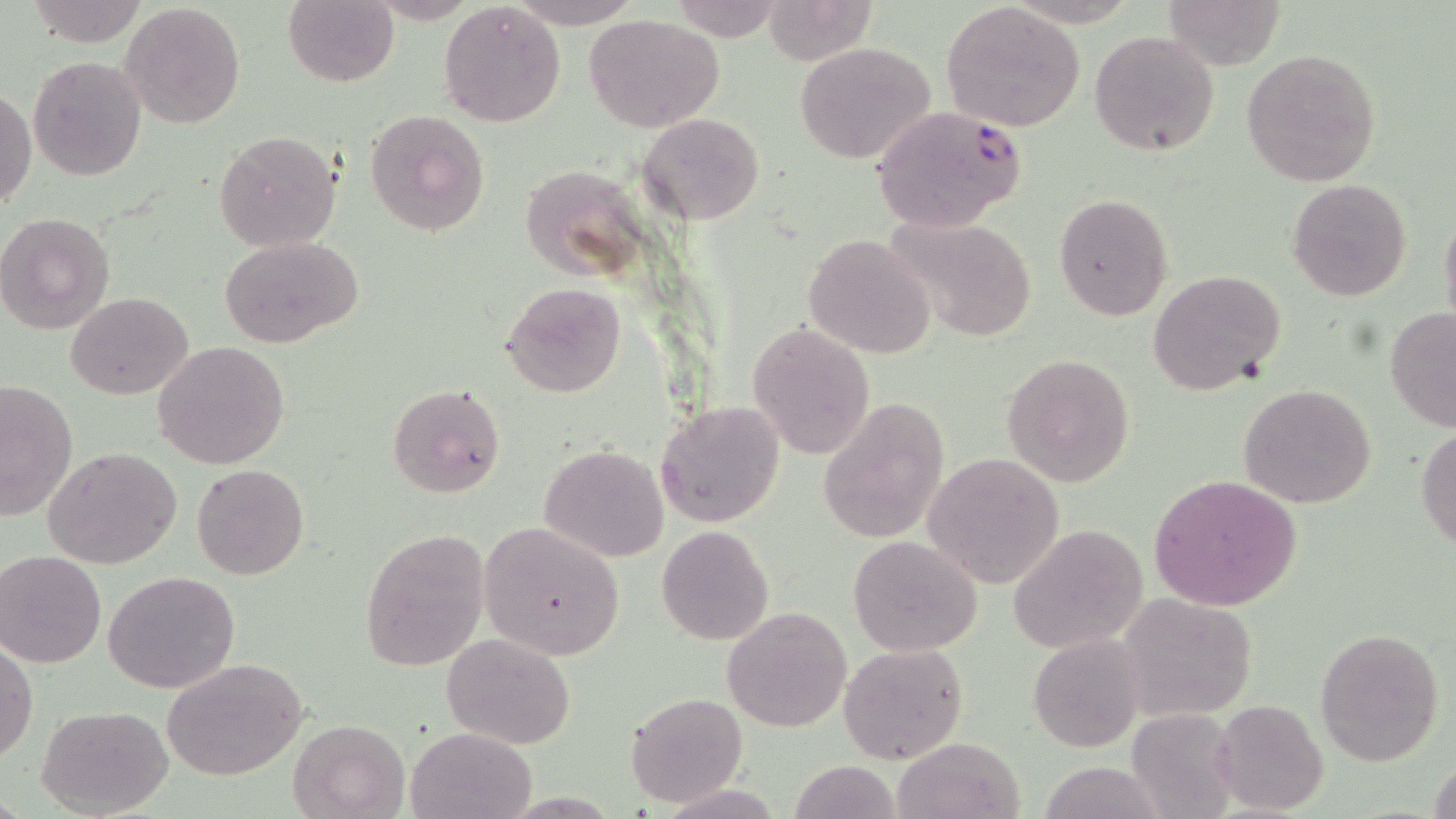
Approximate bounding boxes as (x1,y1)-(x2,y2) corner pairs in pixels. Plasmodium falciparum-infected red blood cell locations: (869,103)-(1028,234). Uninfected red blood cell locations: (25,0)-(150,47), (283,0)-(399,88), (667,0)-(787,43), (763,0)-(880,65), (1163,0)-(1286,69), (505,1)-(646,27), (121,3)-(247,128), (438,3)-(567,128), (940,3)-(1086,132), (583,14)-(726,132), (1088,30)-(1219,156), (792,42)-(936,164), (1242,50)-(1383,186), (27,55)-(147,180), (1,86)-(36,211), (363,110)-(489,236), (638,113)-(764,225), (213,130)-(341,252), (528,162)-(647,283), (1286,177)-(1412,303), (1055,193)-(1174,322), (1439,204)-(1456,340), (1,210)-(117,337), (883,214)-(1038,343), (802,233)-(936,358), (218,236)-(365,352), (1149,269)-(1286,397), (501,283)-(626,398), (67,292)-(193,400), (1383,307)-(1456,432), (747,322)-(876,460), (153,339)-(291,470), (1001,353)-(1135,486), (0,379)-(78,522), (387,383)-(506,498), (1237,383)-(1377,510), (817,396)-(950,543), (653,400)-(786,529), (1416,423)-(1456,552), (539,444)-(668,563), (45,447)-(184,570), (923,452)-(1066,590), (192,464)-(309,581), (1150,473)-(1304,614), (479,522)-(626,661), (657,525)-(774,645), (1010,525)-(1148,654), (358,529)-(490,673), (848,536)-(983,656), (0,550)-(107,668), (102,570)-(241,695), (1120,596)-(1256,718), (723,606)-(852,732), (1313,626)-(1444,767), (443,633)-(575,749), (1028,636)-(1142,751), (0,641)-(37,764), (838,643)-(968,766), (162,658)-(308,780), (626,692)-(747,806), (1210,699)-(1330,816), (37,704)-(173,817), (1124,707)-(1237,818), (288,718)-(408,818), (405,729)-(536,819), (893,737)-(1024,819), (1428,748)-(1456,819), (788,760)-(906,818), (1036,760)-(1172,819). Slide-level diagnosis: Plasmodium falciparum. Single field of view. Light microscopy. 1000x magnification. Thin blood film. Image is 1456×819 pixels. May-Grünwald-Giemsa stain.